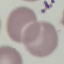
Summary:
  - Malaria status: uninfected
  - Capture: smartphone through the microscope eyepiece
  - Image type: automatically extracted cell patch, resized to 64 × 64 pixels
  - Preparation: thin blood smear
  - Stain: Giemsa